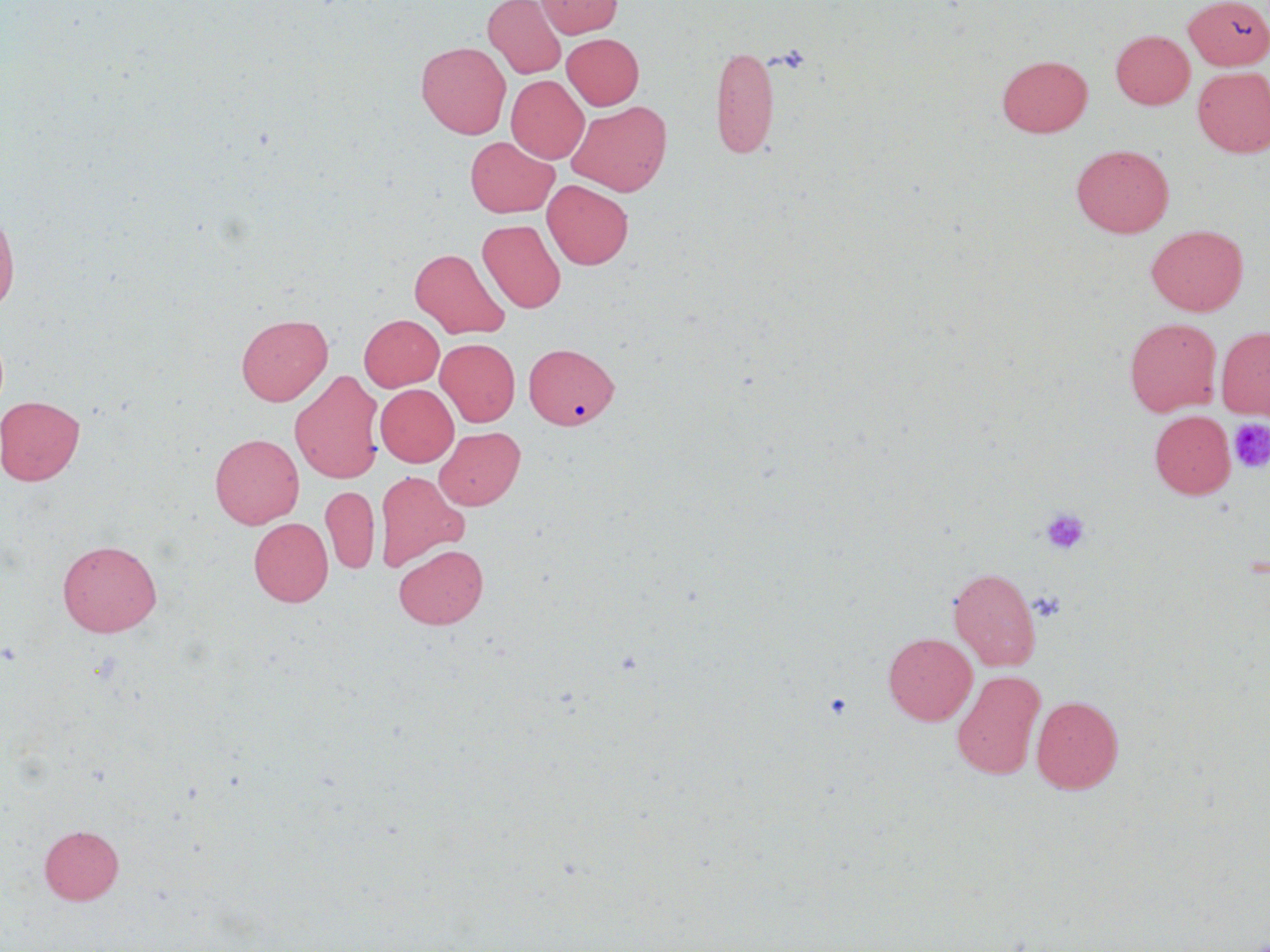
Approximate bounding boxes as [x1, y1, x2, y2] in pixels. Uninfected red blood cell locations: [483, 0, 566, 79], [536, 0, 622, 38], [1184, 0, 1270, 69], [1111, 30, 1194, 109], [562, 33, 644, 110], [416, 41, 511, 138], [709, 43, 779, 158], [997, 55, 1092, 137], [1192, 67, 1270, 157], [506, 75, 589, 163], [566, 100, 672, 196], [464, 136, 559, 217], [1071, 144, 1174, 238], [542, 180, 633, 269], [0, 205, 19, 318], [477, 219, 566, 313], [1147, 225, 1248, 315], [409, 248, 510, 339], [236, 314, 333, 405], [359, 314, 444, 391], [1125, 317, 1222, 415], [1216, 326, 1270, 419], [435, 338, 520, 427], [524, 342, 619, 430], [289, 370, 385, 483], [375, 384, 458, 467], [0, 395, 86, 486], [1149, 410, 1236, 499], [434, 426, 525, 510], [210, 433, 304, 528], [374, 470, 468, 572], [320, 486, 379, 574], [249, 518, 333, 606], [57, 539, 162, 637], [393, 544, 488, 629], [948, 567, 1041, 671], [883, 632, 977, 725], [952, 671, 1045, 780], [1032, 695, 1123, 793], [39, 824, 124, 904]. Platelet locations: [1228, 417, 1270, 474], [1040, 508, 1090, 555], [1029, 589, 1067, 622], [823, 692, 853, 721]. Slide-level diagnosis: no evidence of blood parasites. Optical microscopy. Captured at 1000x magnification. Thin blood smear. Single field of view. Image is 1270×952 pixels. May-Grünwald-Giemsa-stained preparation.